Identify the parasite.
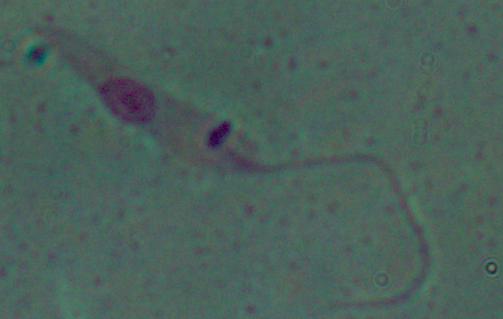
Leishmania.

Summary:
  - Magnification: 1000x
  - Modality: photomicrograph